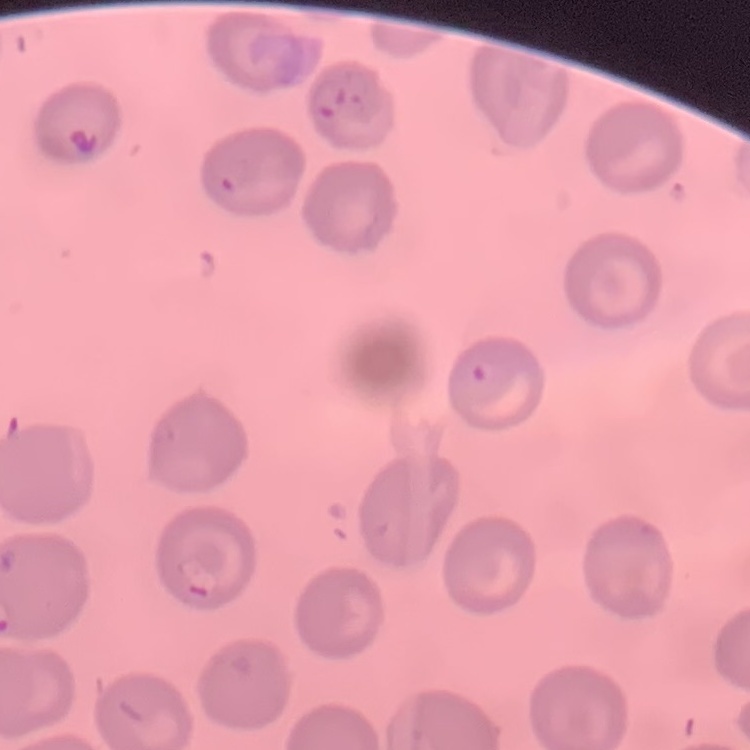

{
  "erythrocyte_morphology": "no rouleaux formation",
  "preparation": "thin blood smear",
  "stain": "Field's or Giemsa",
  "image_type": "square crop of a larger photomicrograph"
}